Locate every blood parasite and identify its species.
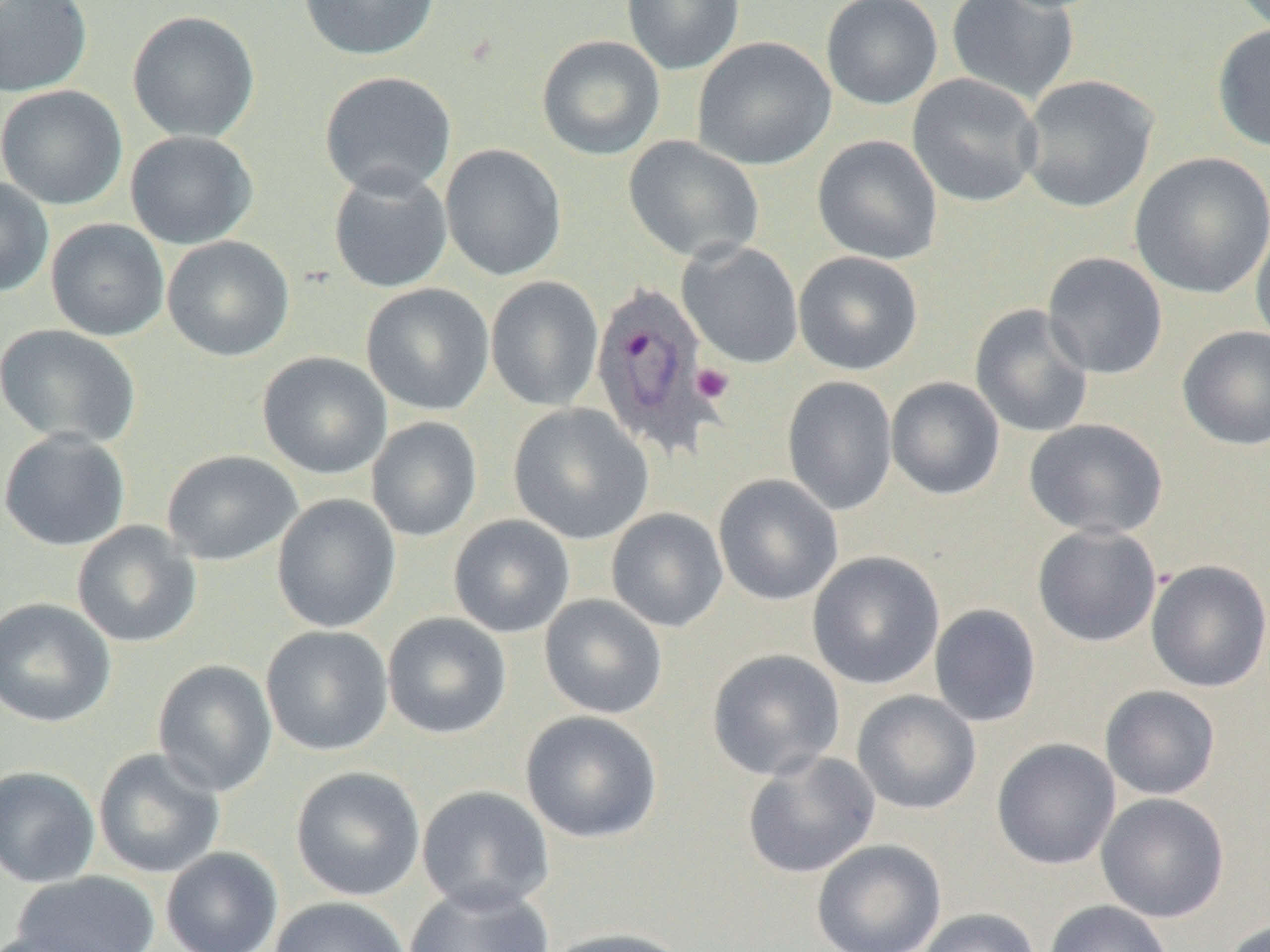
Approximate bounding boxes as (x1,y1)-(x2,y2) corner pairs in pixels.
Plasmodium ovale-infected red blood cells: (589,280)-(722,458).
No Plasmodium falciparum, Plasmodium malariae, Plasmodium vivax, Babesia divergens, or Trypanosoma brucei observed.

Uninfected red blood cell locations: (0,0)-(93,97), (298,0)-(439,60), (622,0)-(745,75), (820,0)-(943,109), (946,0)-(1079,105), (127,11)-(260,143), (1212,22)-(1270,152), (536,35)-(665,160), (692,36)-(837,171), (319,71)-(457,199), (907,73)-(1043,208), (1018,74)-(1160,214), (0,84)-(128,210), (125,130)-(259,250), (812,135)-(943,265), (623,137)-(764,264), (440,144)-(568,281), (1129,152)-(1270,301), (328,167)-(453,294), (0,177)-(54,297), (46,219)-(170,341), (1251,223)-(1270,352), (162,235)-(294,362), (677,241)-(804,368), (793,251)-(924,376), (1042,252)-(1169,380), (485,276)-(604,411), (360,283)-(494,416), (969,303)-(1095,438), (1,324)-(142,448), (1177,326)-(1270,451), (256,351)-(392,479), (782,375)-(898,516), (886,377)-(1005,500), (507,403)-(654,545), (367,417)-(482,542), (1024,418)-(1169,539), (0,428)-(132,551), (161,450)-(303,566), (713,474)-(843,606), (272,493)-(402,634), (606,507)-(728,632), (448,514)-(575,638), (71,521)-(202,648), (1032,523)-(1162,647), (807,551)-(945,690), (1146,559)-(1270,693), (539,594)-(668,719), (0,597)-(116,728), (929,603)-(1041,727), (382,612)-(512,740), (260,625)-(394,757), (706,649)-(846,781), (152,659)-(277,796), (1100,685)-(1221,800), (851,690)-(982,815), (520,711)-(662,844), (991,738)-(1121,870), (93,748)-(226,879), (742,751)-(880,879), (0,765)-(100,888), (290,766)-(426,902), (416,785)-(554,915), (1096,793)-(1230,923), (811,839)-(947,952), (161,847)-(283,952), (12,871)-(161,951), (404,883)-(554,952), (269,896)-(411,952), (1044,899)-(1172,952), (916,907)-(1040,952), (1219,918)-(1270,952), (543,927)-(690,952), (0,929)-(110,952). Platelet locations: (691,364)-(734,404). Slide-level diagnosis: Plasmodium ovale. 1000x magnification. Image is 1270×952 pixels. Optical microscopy. One field of a larger specimen. Thin blood film.